Name the parasite shown.
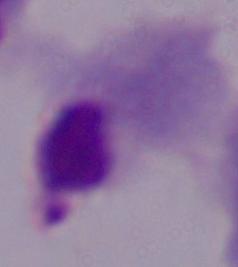
This is a trichomonad.

Summary:
  - Modality: photomicrograph
  - Magnification: 1000x